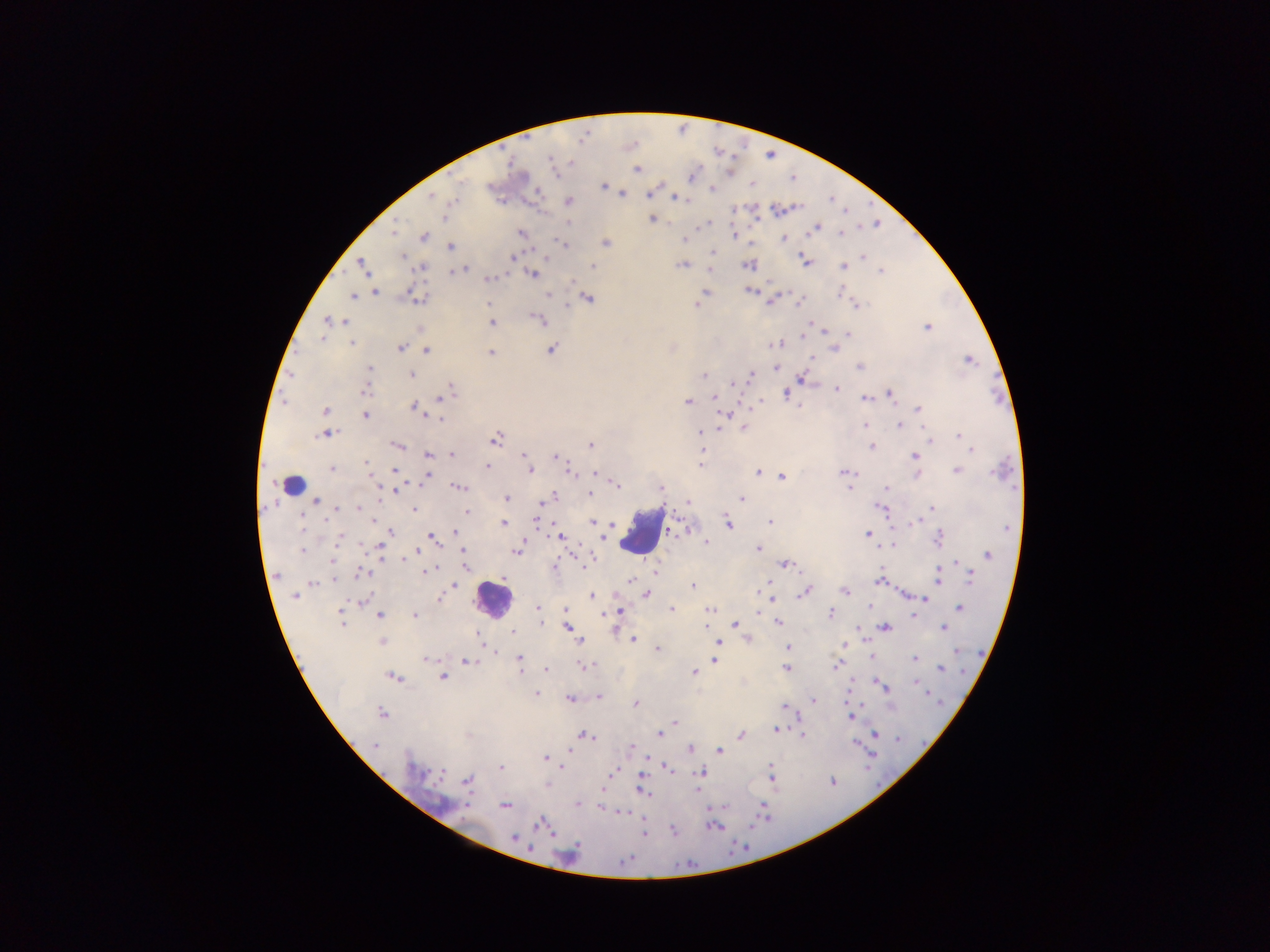

Approximate centers as (x, y) in pixels.
Summary:
  - Malaria parasite locations: (637, 169), (604, 186), (711, 189), (648, 193), (623, 195), (430, 197), (675, 198), (568, 201), (445, 218), (652, 219), (816, 228), (393, 233), (520, 233), (840, 233), (733, 235), (422, 237), (783, 239), (685, 240), (564, 243), (606, 243), (450, 246), (713, 252), (535, 253), (403, 256), (862, 256), (511, 257), (805, 262), (682, 264), (748, 264), (592, 265), (362, 266), (843, 266), (421, 267), (463, 268), (881, 270), (456, 271), (533, 274), (487, 279), (574, 282), (750, 290), (375, 291), (706, 291), (352, 296), (415, 296), (549, 296), (587, 298), (774, 299), (855, 304), (489, 305), (695, 305), (566, 306), (328, 320), (343, 320), (540, 320), (491, 322), (926, 326), (823, 330), (847, 334), (803, 335), (352, 343), (776, 345), (400, 347), (834, 348), (551, 349), (426, 350), (491, 352), (968, 359), (859, 366), (369, 368), (775, 368), (410, 374), (702, 376), (750, 376), (801, 379), (734, 383), (837, 388), (365, 389), (449, 389), (785, 393), (889, 393), (443, 396), (864, 398), (715, 400), (687, 401), (758, 402), (414, 407), (799, 408), (918, 409), (325, 411), (365, 415), (439, 417), (899, 424), (866, 425), (744, 427), (718, 428), (328, 433), (700, 433), (958, 435), (495, 439), (591, 445), (398, 446), (871, 447), (702, 449), (972, 449), (451, 454), (428, 455), (523, 455), (555, 456), (914, 456), (367, 464), (700, 465), (487, 466), (331, 468), (393, 470), (956, 470), (529, 471), (757, 471), (844, 472), (570, 473), (594, 473), (916, 474), (426, 476), (781, 477), (616, 484), (377, 487), (458, 487), (850, 487), (400, 488), (660, 488), (886, 488), (552, 495), (590, 495), (505, 498), (741, 498), (316, 501), (542, 503), (687, 503), (359, 507), (336, 508), (882, 508), (415, 509), (933, 509), (466, 511), (536, 520), (769, 521), (592, 522), (727, 522), (503, 523), (611, 525), (390, 531), (455, 534), (867, 534), (342, 536), (432, 537), (559, 537), (938, 537), (705, 542), (380, 545), (892, 545), (756, 548), (302, 550), (416, 550), (516, 550), (463, 551), (988, 555), (402, 558), (332, 560), (785, 564), (583, 565), (465, 566), (553, 566), (363, 572), (425, 572), (654, 572), (971, 576), (938, 577), (333, 580), (631, 580), (878, 581), (767, 582), (313, 583), (455, 585), (692, 585), (805, 591), (845, 591), (646, 594), (295, 596), (591, 596), (438, 598), (772, 599), (924, 599), (363, 600), (536, 606), (869, 607), (565, 608), (959, 608), (670, 609), (709, 609), (619, 611), (757, 612), (760, 613), (829, 613), (379, 615), (414, 615), (915, 615), (341, 617), (777, 622), (343, 623), (541, 623), (734, 624), (707, 625), (568, 627), (885, 627), (944, 628), (613, 630), (512, 632), (482, 639), (633, 639), (749, 639), (382, 641), (581, 641), (718, 642), (843, 645), (656, 648), (788, 648), (495, 653), (871, 656), (519, 657), (916, 658), (427, 659), (714, 660), (467, 661), (839, 661), (836, 666), (582, 667), (940, 668), (545, 669), (786, 669), (693, 672), (394, 676), (442, 676), (880, 683), (535, 693), (924, 693), (598, 696), (570, 698), (813, 700), (636, 702), (785, 707), (382, 714), (852, 717), (675, 723), (775, 729), (660, 733), (874, 733), (802, 734), (583, 735), (740, 735), (854, 742), (375, 746), (630, 747), (689, 748), (566, 751), (718, 751), (544, 759), (771, 765), (561, 766), (501, 767), (665, 767), (611, 772), (699, 772), (771, 777), (468, 780), (547, 784), (641, 788), (602, 791), (647, 794), (577, 804), (504, 805), (601, 806), (618, 811), (624, 812), (540, 823), (513, 838)
  - Leukocyte locations: (293, 484), (643, 529), (493, 600)
  - Image size: 1270×952 pixels
  - Country: Ghana
  - Capture: mobile-phone photograph through a microscope
  - Field of view: single
  - Preparation: thick blood film